Identify the parasite.
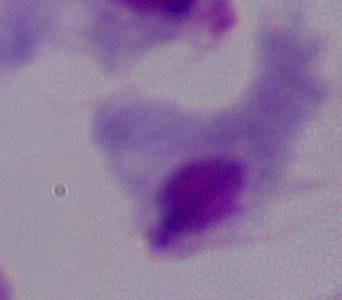
This is a trichomonad.

Micrograph. Captured at 1000x magnification.